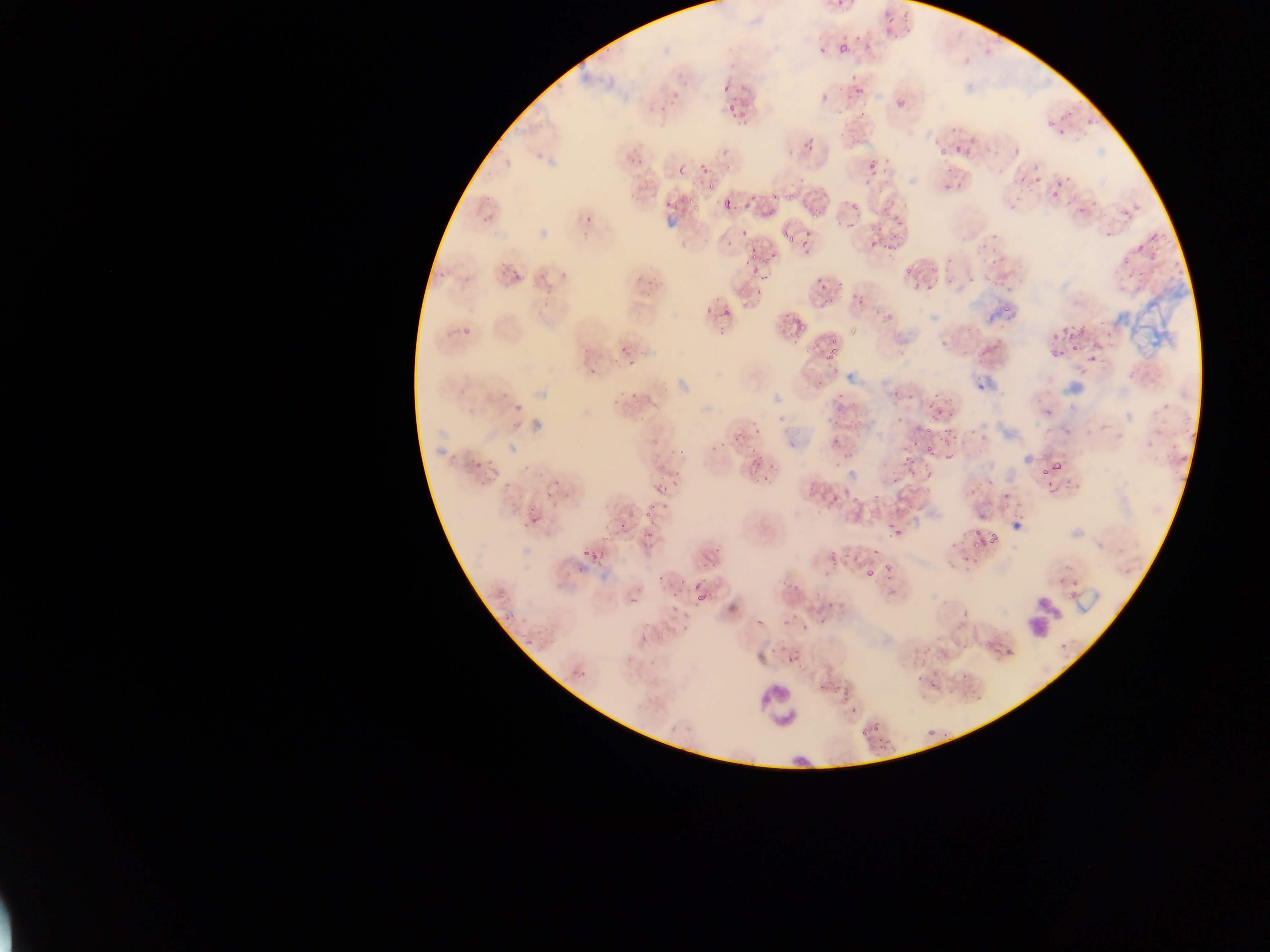
Approximate bounding boxes as (left, top, right, bottom) in pixels. Plasmodium parasite locations (subset; some below the resolvable size): (839, 43, 847, 55), (723, 85, 730, 93), (670, 93, 683, 98), (730, 102, 735, 112), (658, 106, 669, 114), (741, 106, 746, 121), (1015, 146, 1022, 154), (939, 151, 948, 156), (1034, 163, 1042, 171), (679, 165, 685, 176), (947, 169, 955, 172), (703, 170, 711, 176), (1064, 175, 1073, 183), (1021, 176, 1027, 184), (690, 195, 696, 203), (724, 196, 732, 209), (851, 202, 860, 210), (1079, 205, 1085, 216), (483, 215, 489, 225), (584, 215, 592, 223), (804, 233, 812, 238), (787, 235, 795, 242), (800, 243, 808, 248), (1137, 243, 1144, 252), (752, 253, 758, 261), (744, 258, 749, 268), (751, 267, 760, 275), (817, 275, 823, 284), (464, 276, 471, 285), (1006, 281, 1011, 289), (712, 293, 723, 304), (706, 308, 712, 316), (721, 310, 729, 320), (459, 325, 474, 336), (831, 336, 837, 344), (1051, 348, 1057, 358), (827, 352, 833, 360), (628, 360, 636, 365), (588, 366, 597, 375), (631, 392, 639, 400), (837, 392, 845, 399), (893, 392, 901, 397), (613, 397, 621, 405), (946, 397, 954, 403), (928, 399, 934, 407), (897, 416, 903, 425), (749, 421, 759, 429), (916, 421, 923, 431), (944, 426, 950, 434), (751, 430, 760, 437), (943, 434, 952, 441), (980, 434, 985, 442), (835, 437, 843, 443), (913, 439, 922, 446), (721, 441, 730, 447), (927, 444, 934, 452), (712, 445, 720, 451), (679, 447, 685, 457), (749, 448, 757, 454), (848, 453, 857, 459), (944, 453, 952, 463), (1052, 460, 1063, 470), (832, 461, 844, 468), (901, 461, 909, 468), (769, 466, 778, 471), (480, 477, 489, 488), (762, 477, 771, 482), (894, 479, 902, 485), (986, 480, 994, 483), (1048, 481, 1052, 490), (656, 483, 663, 492), (969, 490, 977, 495), (872, 495, 880, 500), (814, 510, 822, 515), (645, 511, 653, 519), (621, 522, 626, 531), (893, 530, 901, 537), (990, 532, 998, 545), (973, 541, 979, 549), (715, 545, 722, 553), (583, 547, 590, 555), (703, 559, 708, 570), (709, 559, 716, 570), (885, 563, 893, 570), (865, 569, 875, 577), (657, 576, 665, 584), (677, 580, 685, 584), (697, 589, 707, 603), (759, 684, 796, 733) | approximate (x, y) pixel centers of objects too small to bound: (734, 117), (1088, 122), (1061, 129), (958, 149), (702, 165), (1037, 180), (1060, 184), (711, 187), (947, 188), (1055, 193), (775, 196), (754, 197), (669, 204), (697, 207), (769, 215), (744, 231), (729, 243), (752, 251), (770, 256), (564, 273), (442, 274), (502, 274), (763, 278), (822, 289), (759, 292), (1006, 309), (802, 325), (1065, 331), (1055, 336), (624, 347), (1074, 347), (834, 351), (1062, 354), (1093, 358), (938, 395), (911, 396), (1048, 412), (939, 413), (950, 414), (928, 430), (973, 430), (907, 457), (479, 464), (1044, 471), (677, 473), (665, 490), (1007, 495), (855, 499), (535, 521), (526, 523), (890, 526), (650, 532), (978, 532), (874, 550), (832, 552), (697, 584), (508, 619), (529, 643), (876, 727), (865, 733). Leukocyte locations: (1023, 596, 1063, 637), (791, 749, 815, 774). Artifact (stain precipitate or debris) locations: (1117, 287, 1192, 348). Thin blood smear. Mobile-phone photograph taken through the microscope. Collected in Ghana. Image is 1270×952 pixels. Single field of view.